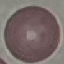
result = no malaria parasites seen
preparation = thin smear
capture = smartphone through the microscope eyepiece
stain = Giemsa
image type = cell patch, automatically extracted from a larger field of view and resized to 64 × 64 pixels